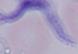

identification = trypanosome
modality = photomicrograph
magnification = 1000x